Assess this cell for malaria.
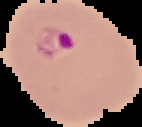

Parasitized.

preparation: thin blood film
image_size: 142×127 pixels
image_type: segmented cell region on a black background